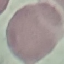 Result: negative for malaria parasites. Thin blood smear. Giemsa-stained preparation. Automatically extracted cell patch, resized to 64 × 64 pixels. Photographed with a smartphone camera at the microscope eyepiece.